Outline each Plasmodium falciparum-infected red blood cell.
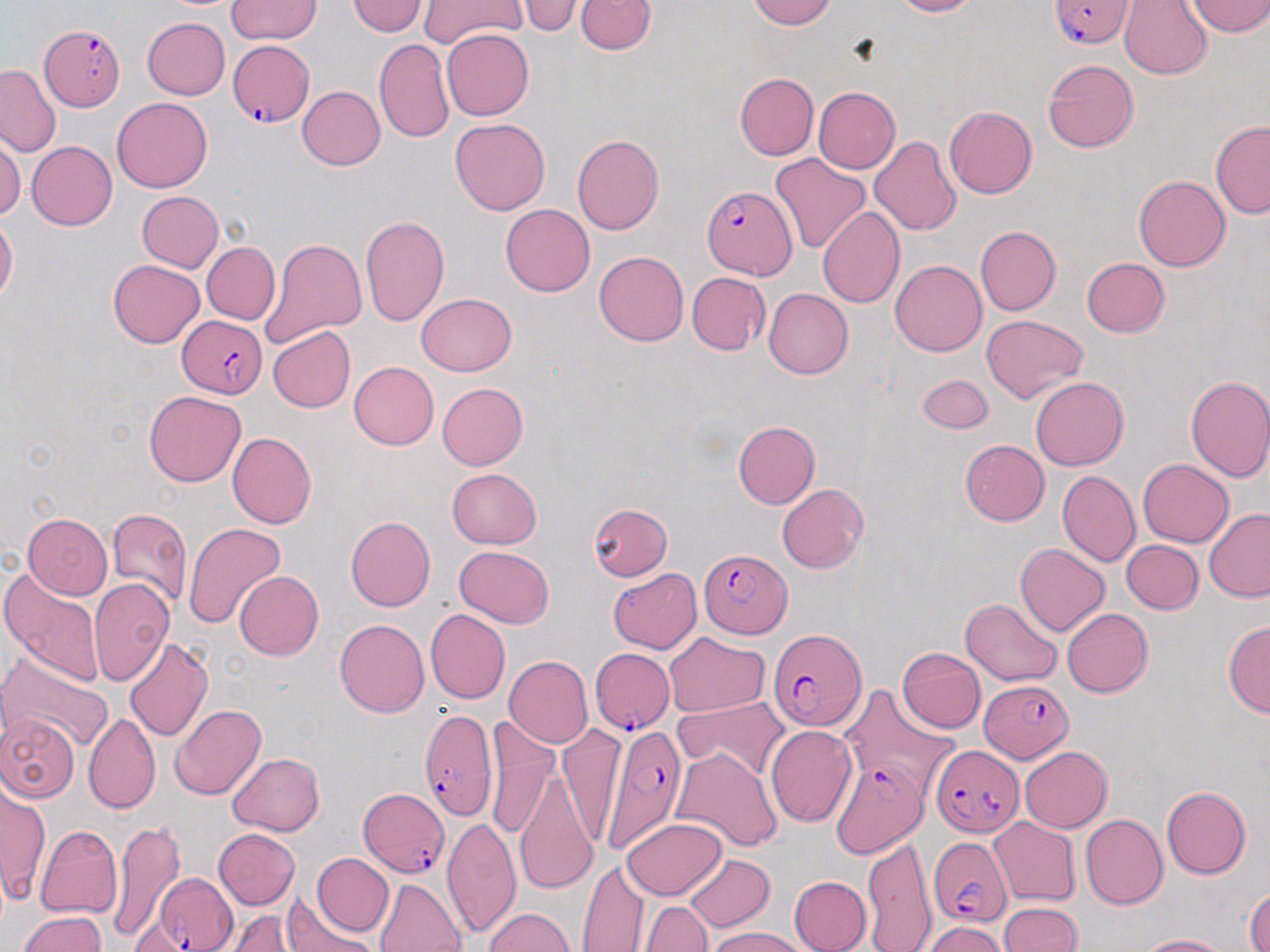
Approximate bounding boxes as (x1, y1, x2, y2) in pixels.
Plasmodium falciparum-infected red blood cells: (1047, 1, 1134, 50), (42, 24, 126, 110), (225, 42, 313, 128), (702, 184, 798, 277), (175, 318, 267, 397), (701, 547, 795, 638), (768, 628, 866, 734), (587, 651, 675, 735), (978, 678, 1076, 765), (418, 708, 499, 819), (596, 722, 686, 853), (932, 745, 1021, 837), (830, 755, 928, 855), (358, 787, 450, 877), (929, 836, 1011, 927), (147, 872, 240, 952).

Uninfected red blood cell locations: (226, 0, 321, 43), (346, 0, 428, 39), (417, 0, 529, 46), (521, 0, 579, 37), (577, 0, 654, 56), (740, 0, 842, 30), (885, 0, 980, 18), (1119, 0, 1213, 77), (1189, 0, 1270, 38), (141, 18, 231, 101), (439, 28, 534, 121), (375, 40, 453, 142), (1041, 58, 1138, 155), (0, 67, 63, 158), (735, 73, 817, 160), (296, 85, 384, 171), (812, 85, 899, 173), (111, 98, 213, 194), (944, 105, 1036, 200), (450, 119, 551, 214), (1210, 120, 1270, 219), (573, 134, 664, 236), (869, 135, 960, 238), (0, 137, 22, 224), (24, 140, 116, 231), (768, 153, 871, 255), (1133, 175, 1230, 271), (136, 191, 225, 272), (499, 203, 594, 296), (818, 207, 904, 308), (359, 213, 450, 328), (0, 216, 17, 311), (976, 225, 1060, 315), (261, 235, 367, 347), (203, 241, 279, 324), (593, 249, 689, 348), (891, 258, 989, 357), (1080, 258, 1170, 337), (107, 260, 204, 347), (685, 273, 771, 355), (763, 290, 852, 377), (419, 291, 517, 375), (980, 314, 1090, 403), (266, 325, 356, 413), (347, 362, 438, 450), (917, 374, 993, 434), (1184, 374, 1270, 484), (1028, 376, 1130, 471), (437, 381, 527, 468), (144, 391, 245, 487), (733, 420, 819, 508), (227, 432, 316, 528), (961, 439, 1049, 525), (1136, 458, 1231, 547), (446, 468, 544, 549), (1059, 470, 1140, 568), (777, 483, 869, 572), (591, 503, 671, 582), (106, 507, 191, 609), (1203, 508, 1270, 601), (22, 513, 112, 599), (344, 516, 434, 612), (182, 523, 286, 629), (1123, 539, 1202, 614), (1014, 543, 1110, 636), (454, 545, 555, 628), (0, 565, 104, 686), (608, 569, 703, 655), (232, 570, 323, 661), (89, 578, 175, 688), (961, 598, 1062, 685), (1063, 608, 1153, 697), (424, 610, 509, 705), (333, 617, 431, 719), (1223, 620, 1270, 718), (123, 633, 213, 745), (664, 633, 768, 716), (897, 646, 985, 735), (503, 653, 592, 746), (1, 658, 112, 753), (840, 685, 961, 800), (675, 696, 786, 782), (169, 703, 266, 801), (2, 712, 79, 803), (82, 712, 161, 812), (484, 714, 559, 839), (766, 725, 858, 828), (1018, 744, 1112, 832), (672, 749, 781, 856), (227, 753, 326, 837), (516, 760, 598, 895), (1, 783, 49, 910), (1160, 785, 1250, 879), (1081, 815, 1167, 908), (619, 816, 727, 900), (106, 817, 189, 941), (989, 817, 1080, 906), (442, 818, 518, 934), (38, 823, 124, 916), (213, 829, 300, 909), (862, 837, 934, 952), (312, 853, 394, 936), (683, 853, 772, 933), (580, 860, 646, 949), (788, 874, 871, 952), (375, 877, 465, 952), (1244, 886, 1270, 952), (645, 898, 712, 952), (283, 899, 370, 952), (997, 900, 1081, 952), (231, 908, 292, 952), (483, 908, 577, 952), (16, 910, 109, 952), (921, 922, 1005, 952), (706, 927, 808, 952), (1134, 931, 1235, 951). Slide-level diagnosis: Plasmodium falciparum. Captured at 1000x magnification. Single field of view. Image is 1270×952 pixels. Thin blood film. Optical microscopy. May-Grünwald-Giemsa-stained preparation.